Assess the morphology of the erythrocytes.
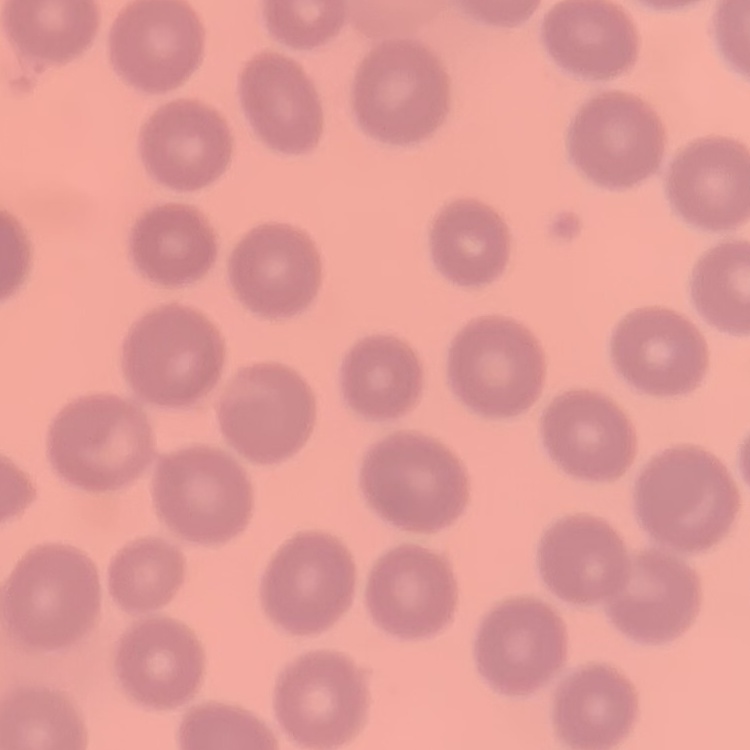

No rouleaux formation.

One tile cut from a larger photomicrograph. Stained with either Field's or Giemsa. Thin blood smear.